Assess this cell for malaria.
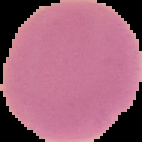
It is uninfected.

Cell region segmented out of the field of view; the surrounding area is masked to black. From a thin blood film. Image is 142×142 pixels.